Find the cells and give the type of each one.
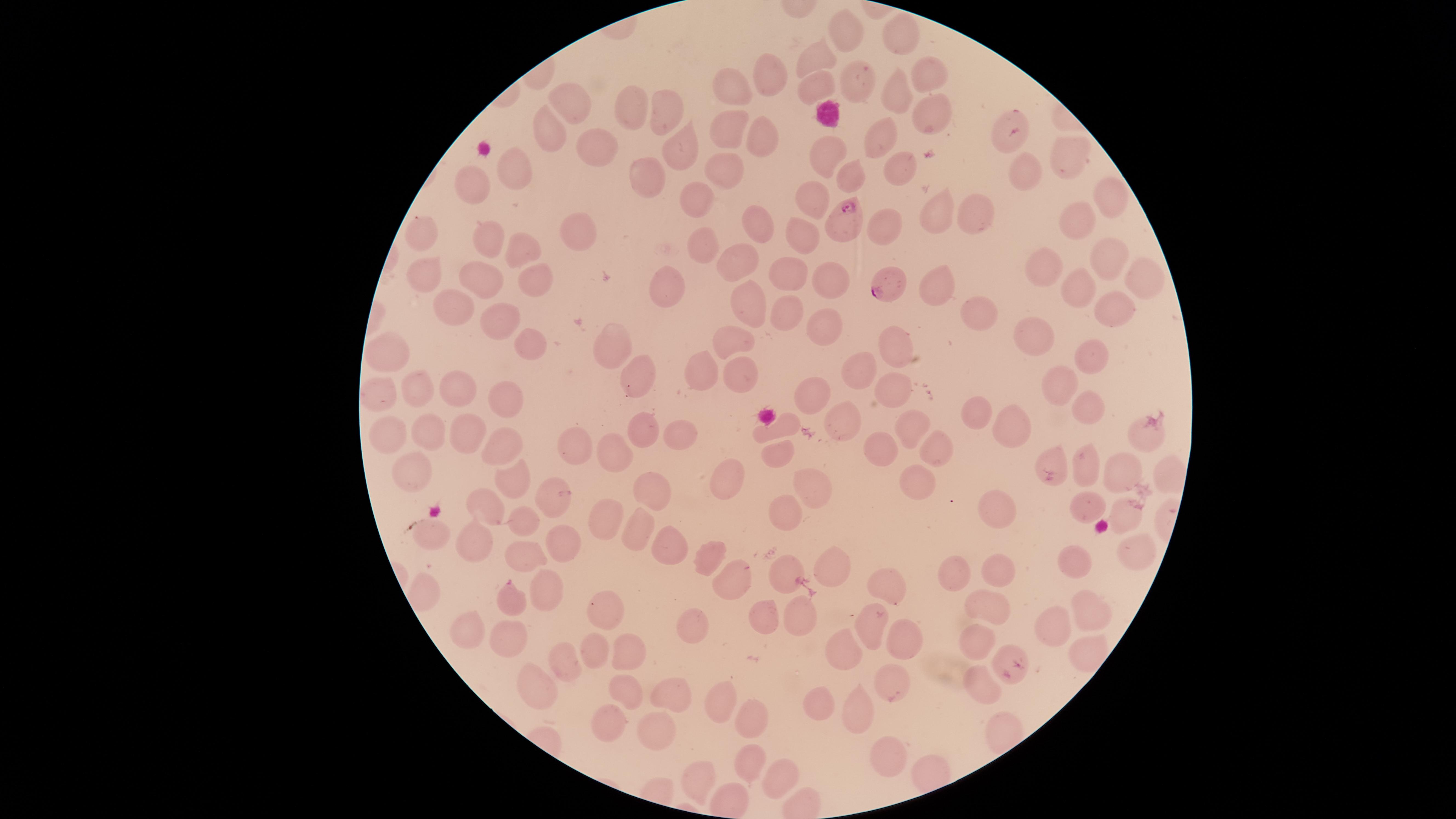
Approximate marker points as {x, y} in pixels.
Parasitized red blood cells: {1010, 132}, {847, 214}, {890, 285}.
Uninfected red blood cells: {905, 32}, {848, 33}, {818, 57}, {926, 73}, {770, 77}, {854, 80}, {815, 86}, {731, 90}, {901, 90}, {570, 107}, {631, 107}, {668, 113}, {933, 118}, {733, 130}, {550, 134}, {885, 139}, {761, 140}, {604, 143}, {681, 148}, {829, 152}, {1069, 154}, {900, 168}, {518, 170}, {727, 171}, {850, 175}, {1027, 175}, {645, 177}, {473, 185}, {1112, 195}, {697, 196}, {813, 201}, {976, 215}, {938, 216}, {1075, 220}, {754, 221}, {895, 224}, {418, 230}, {577, 230}, {804, 233}, {485, 237}, {702, 248}, {521, 250}, {739, 258}, {1105, 260}, {1043, 268}, {428, 272}, {786, 273}, {482, 278}, {830, 278}, {673, 279}, {1142, 280}, {534, 283}, {1076, 285}, {936, 287}, {450, 301}, {742, 303}, {1109, 306}, {780, 313}, {494, 316}, {975, 317}, {820, 325}, {1030, 334}, {530, 339}, {610, 342}, {736, 342}, {896, 350}, {1094, 352}, {389, 354}, {862, 370}, {739, 374}, {698, 376}, {634, 378}, {1056, 381}, {453, 385}, {421, 389}, {897, 390}, {816, 391}, {378, 394}, {505, 398}, {1086, 405}, {971, 409}, {845, 417}, {1008, 425}, {783, 428}, {911, 429}, {645, 430}, {468, 433}, {679, 433}, {429, 434}, {1143, 435}, {389, 438}, {579, 445}, {498, 446}, {612, 447}, {882, 447}, {932, 448}, {775, 452}, {1054, 460}, {1085, 466}, {414, 471}, {1125, 473}, {1166, 475}, {725, 479}, {916, 485}, {511, 487}, {653, 487}, {807, 490}, {547, 495}, {487, 502}, {1083, 507}, {603, 512}, {996, 512}, {1129, 514}, {785, 518}, {527, 523}, {633, 528}, {433, 535}, {568, 540}, {475, 545}, {1136, 546}, {658, 547}, {707, 553}, {525, 560}, {1077, 562}, {827, 568}, {783, 572}, {996, 574}, {956, 576}, {727, 582}, {427, 589}, {888, 589}, {548, 590}, {511, 600}, {605, 606}, {1092, 606}, {989, 610}, {762, 618}, {797, 618}, {696, 625}, {868, 627}, {463, 629}, {1057, 633}, {508, 638}, {977, 638}, {900, 644}, {845, 646}, {1082, 649}, {627, 650}, {591, 653}, {1014, 655}, {563, 664}, {896, 682}, {985, 684}, {626, 688}, {536, 692}, {671, 696}, {821, 701}, {717, 708}, {857, 712}, {746, 717}, {607, 726}, {658, 729}, {884, 750}, {745, 764}, {703, 777}, {780, 779}.
White blood cells: {827, 113}.

One field of view of the specimen. Image is 1456×819 pixels. Species: Plasmodium falciparum. Smartphone photograph through the microscope eyepiece. Thin smear of blood. Giemsa-stained preparation. The visible region is circular.